Give the preparation type.
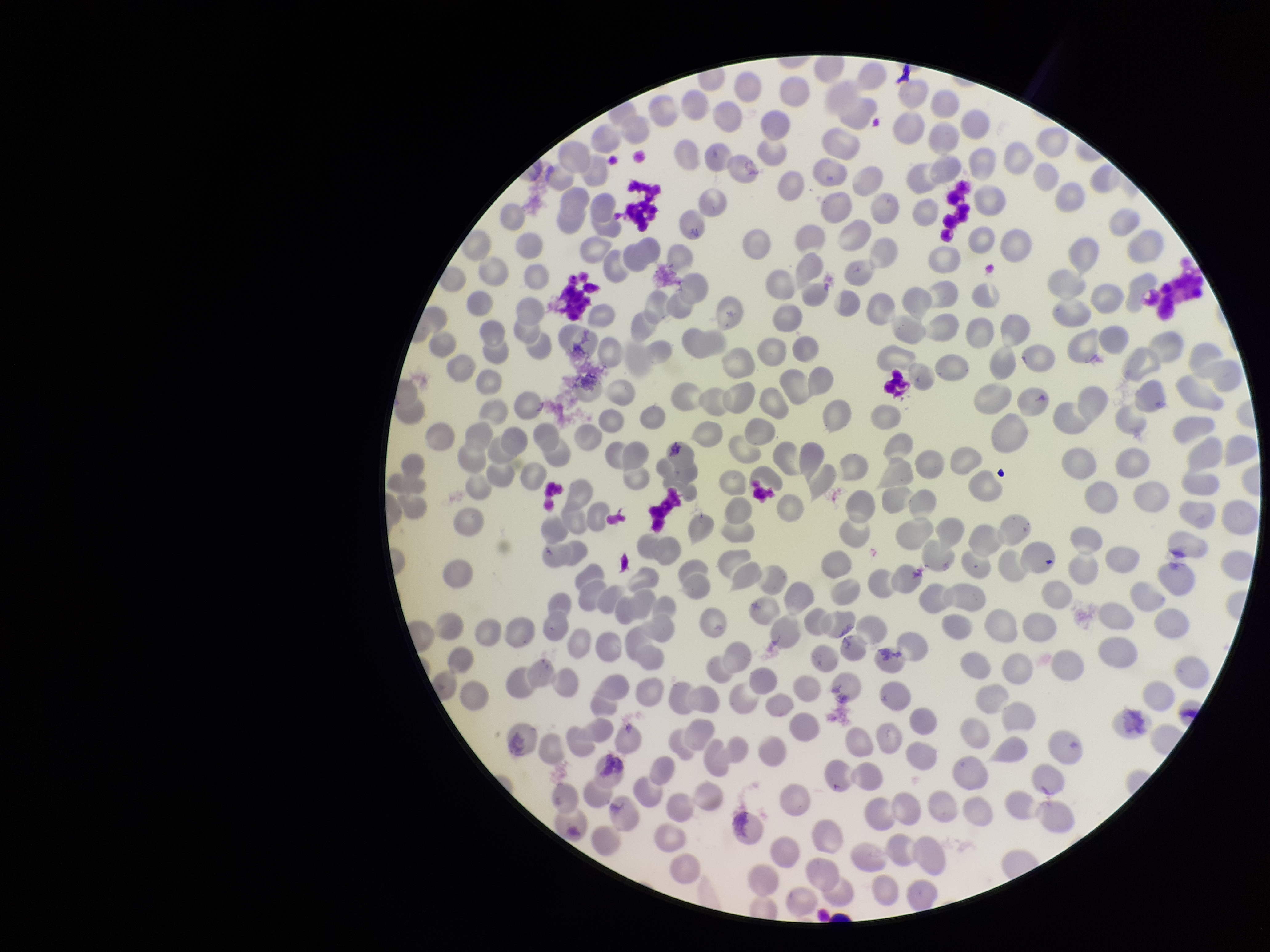

A thin smear.

Summary:
  - Capture: smartphone photograph through the microscope eyepiece
  - Image size: 1270×952 pixels
  - Stain: Giemsa
  - Parasitized red blood cell count: 0
  - Red blood cell count: 336
  - Field of view: single
  - Parasitized red blood cells: none identified
  - Patient malaria status: negative